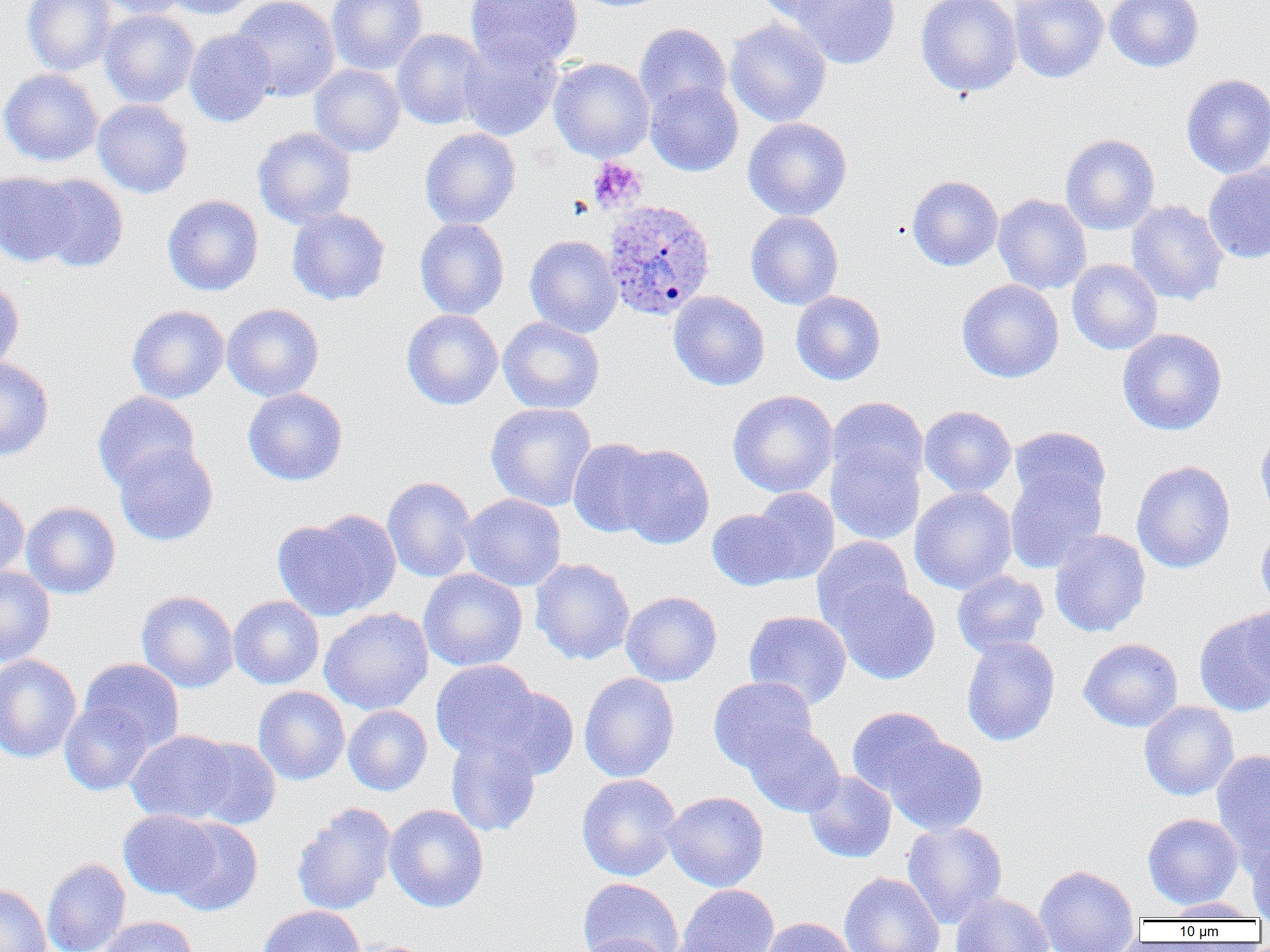 Approximate bounding boxes as named x1/y1/x2/y2 corners in pixels. Platelet locations: (x1=588, y1=157, x2=647, y2=212). Plasmodium ovale-infected red blood cell locations: (x1=601, y1=199, x2=716, y2=321). Uninfected red blood cell locations: (x1=22, y1=0, x2=116, y2=76), (x1=92, y1=0, x2=191, y2=19), (x1=162, y1=0, x2=259, y2=20), (x1=231, y1=0, x2=340, y2=101), (x1=327, y1=0, x2=428, y2=75), (x1=465, y1=0, x2=582, y2=72), (x1=754, y1=0, x2=852, y2=24), (x1=791, y1=0, x2=901, y2=69), (x1=915, y1=0, x2=1022, y2=97), (x1=1010, y1=0, x2=1108, y2=83), (x1=1105, y1=0, x2=1204, y2=72), (x1=100, y1=10, x2=199, y2=108), (x1=724, y1=19, x2=832, y2=127), (x1=634, y1=23, x2=731, y2=115), (x1=184, y1=29, x2=276, y2=127), (x1=391, y1=29, x2=489, y2=129), (x1=458, y1=36, x2=563, y2=141), (x1=549, y1=57, x2=654, y2=162), (x1=309, y1=64, x2=405, y2=157), (x1=0, y1=68, x2=103, y2=166), (x1=1181, y1=73, x2=1270, y2=178), (x1=645, y1=80, x2=743, y2=176), (x1=92, y1=99, x2=194, y2=198), (x1=742, y1=117, x2=853, y2=221), (x1=252, y1=127, x2=357, y2=229), (x1=419, y1=128, x2=521, y2=230), (x1=1060, y1=133, x2=1160, y2=235), (x1=1203, y1=163, x2=1270, y2=263), (x1=0, y1=170, x2=80, y2=267), (x1=33, y1=174, x2=129, y2=273), (x1=907, y1=174, x2=1003, y2=271), (x1=162, y1=194, x2=264, y2=296), (x1=993, y1=194, x2=1091, y2=295), (x1=1126, y1=200, x2=1228, y2=306), (x1=287, y1=208, x2=390, y2=305), (x1=746, y1=211, x2=844, y2=310), (x1=415, y1=218, x2=509, y2=319), (x1=524, y1=235, x2=622, y2=338), (x1=1067, y1=259, x2=1163, y2=355), (x1=0, y1=276, x2=24, y2=374), (x1=957, y1=279, x2=1064, y2=383), (x1=668, y1=291, x2=770, y2=391), (x1=791, y1=291, x2=886, y2=385), (x1=221, y1=303, x2=324, y2=401), (x1=127, y1=305, x2=229, y2=404), (x1=402, y1=309, x2=503, y2=410), (x1=498, y1=316, x2=605, y2=414), (x1=1117, y1=327, x2=1228, y2=436), (x1=0, y1=356, x2=54, y2=461), (x1=242, y1=387, x2=348, y2=486), (x1=727, y1=390, x2=838, y2=498), (x1=92, y1=391, x2=200, y2=492), (x1=827, y1=397, x2=928, y2=490), (x1=485, y1=403, x2=597, y2=511), (x1=919, y1=405, x2=1017, y2=498), (x1=1255, y1=422, x2=1270, y2=524), (x1=1009, y1=426, x2=1111, y2=514), (x1=567, y1=438, x2=663, y2=538), (x1=826, y1=441, x2=925, y2=545), (x1=114, y1=443, x2=219, y2=546), (x1=613, y1=443, x2=714, y2=550), (x1=1131, y1=460, x2=1235, y2=574), (x1=1004, y1=466, x2=1107, y2=574), (x1=382, y1=476, x2=477, y2=583), (x1=909, y1=487, x2=1017, y2=594), (x1=0, y1=488, x2=30, y2=581), (x1=748, y1=488, x2=839, y2=585), (x1=458, y1=493, x2=567, y2=592), (x1=22, y1=501, x2=121, y2=599), (x1=707, y1=508, x2=797, y2=590), (x1=272, y1=512, x2=401, y2=622), (x1=1256, y1=521, x2=1270, y2=616), (x1=1049, y1=529, x2=1151, y2=638), (x1=812, y1=536, x2=913, y2=633), (x1=530, y1=558, x2=635, y2=665), (x1=0, y1=566, x2=55, y2=666), (x1=418, y1=568, x2=528, y2=671), (x1=951, y1=570, x2=1049, y2=658), (x1=828, y1=578, x2=942, y2=685), (x1=137, y1=590, x2=238, y2=692), (x1=621, y1=591, x2=722, y2=686), (x1=228, y1=596, x2=325, y2=689), (x1=1245, y1=602, x2=1269, y2=689), (x1=319, y1=608, x2=434, y2=715), (x1=1193, y1=609, x2=1270, y2=717), (x1=743, y1=610, x2=852, y2=709), (x1=961, y1=636, x2=1060, y2=746), (x1=1078, y1=638, x2=1183, y2=732), (x1=0, y1=654, x2=82, y2=764), (x1=79, y1=658, x2=184, y2=752), (x1=431, y1=659, x2=543, y2=762), (x1=579, y1=672, x2=680, y2=782), (x1=708, y1=676, x2=817, y2=773), (x1=253, y1=686, x2=350, y2=785), (x1=482, y1=686, x2=578, y2=780), (x1=1139, y1=700, x2=1239, y2=801), (x1=59, y1=702, x2=154, y2=795), (x1=343, y1=705, x2=432, y2=795), (x1=846, y1=706, x2=948, y2=797), (x1=743, y1=722, x2=845, y2=817), (x1=126, y1=730, x2=238, y2=824), (x1=445, y1=734, x2=541, y2=837), (x1=884, y1=736, x2=988, y2=836), (x1=189, y1=737, x2=281, y2=830), (x1=1211, y1=749, x2=1270, y2=862), (x1=803, y1=771, x2=896, y2=863), (x1=576, y1=773, x2=682, y2=881), (x1=662, y1=791, x2=769, y2=892), (x1=291, y1=802, x2=396, y2=916), (x1=384, y1=804, x2=489, y2=912), (x1=118, y1=809, x2=221, y2=900), (x1=1142, y1=812, x2=1243, y2=909), (x1=166, y1=817, x2=263, y2=916), (x1=902, y1=821, x2=1007, y2=928), (x1=1246, y1=830, x2=1270, y2=920), (x1=41, y1=858, x2=131, y2=952), (x1=1034, y1=864, x2=1140, y2=952), (x1=839, y1=872, x2=945, y2=952), (x1=578, y1=877, x2=684, y2=952), (x1=0, y1=883, x2=51, y2=952), (x1=675, y1=884, x2=779, y2=952), (x1=950, y1=892, x2=1055, y2=952), (x1=1160, y1=898, x2=1261, y2=920), (x1=258, y1=905, x2=366, y2=952), (x1=96, y1=916, x2=199, y2=952), (x1=758, y1=917, x2=858, y2=952), (x1=576, y1=933, x2=676, y2=952), (x1=343, y1=939, x2=440, y2=952). Slide-level diagnosis: Plasmodium ovale. One field of a larger specimen. Light microscopy. Image is 1270×952 pixels. Captured at 1000x magnification. Thin blood smear.